Outline malaria parasites and classify them by life-cycle stage.
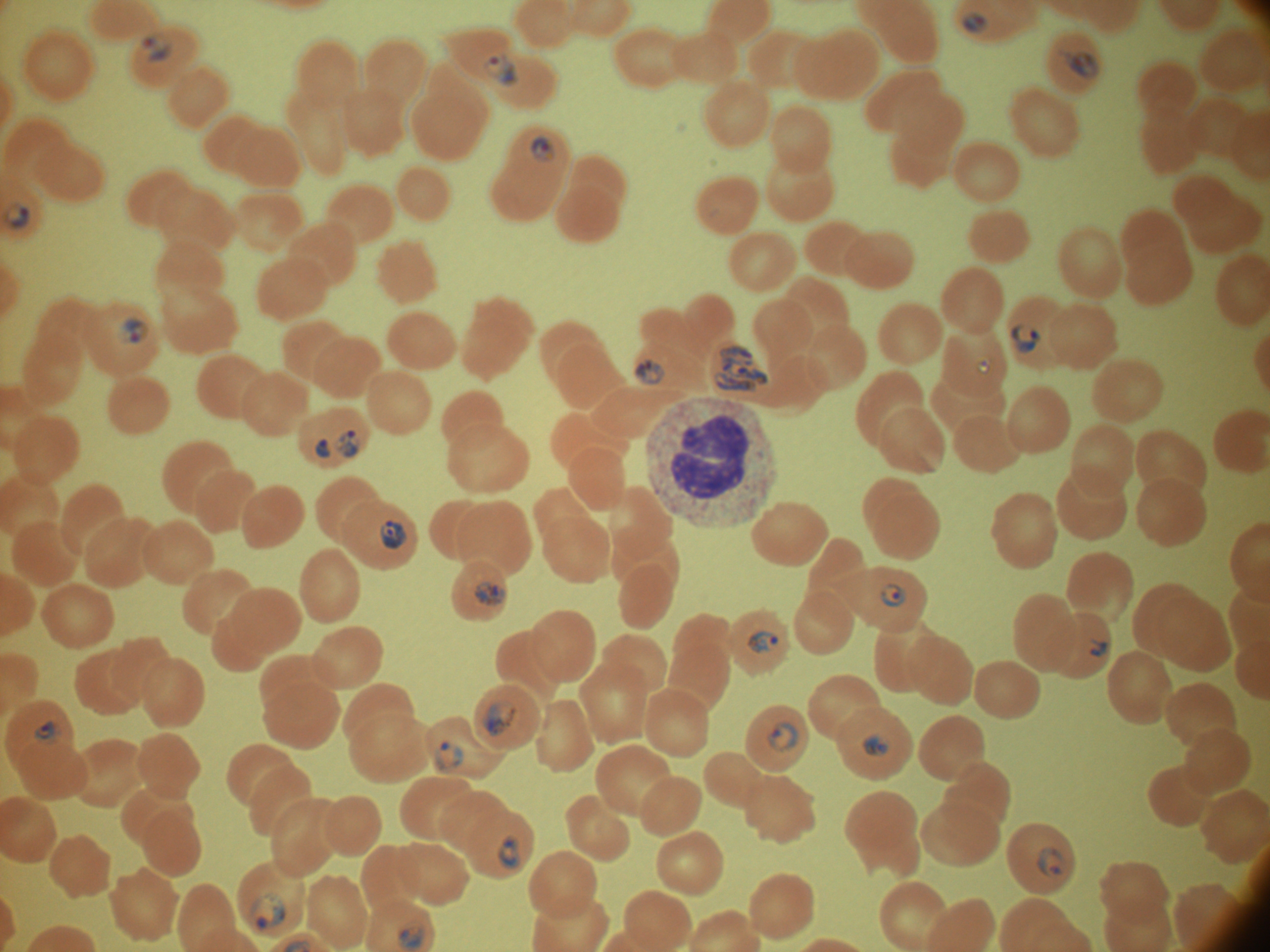
Approximate bounding boxes as [x1, y1, x2, y2] in pixels, from the source annotation, which is not necessarily exhaustive.
Ring forms: [962, 11, 990, 35], [140, 36, 173, 63], [1057, 48, 1100, 79], [483, 53, 519, 87], [529, 135, 556, 164], [1, 202, 30, 229], [117, 316, 148, 344], [1009, 322, 1041, 354], [635, 357, 665, 385], [976, 359, 992, 375], [336, 429, 360, 458], [314, 439, 331, 458], [879, 583, 908, 608], [747, 630, 779, 653], [1090, 639, 1108, 657], [33, 720, 61, 744], [766, 720, 800, 752], [862, 732, 891, 756], [435, 741, 464, 772], [498, 835, 520, 869], [1037, 846, 1067, 881], [248, 893, 286, 931], [395, 921, 425, 951].
Trophozoites: [711, 345, 771, 394], [378, 520, 407, 550], [474, 580, 507, 607], [483, 701, 518, 736].

Summary:
  - Life-cycle stages among the annotated parasites: ring form, trophozoite
  - Magnification: 100x
  - Image size: 1270×952 pixels
  - Stain: Giemsa
  - Microscope: Leica DM2000 with built-in camera
  - Species: Plasmodium falciparum
  - Preparation: thin blood smear
  - Field of view: one from this slide